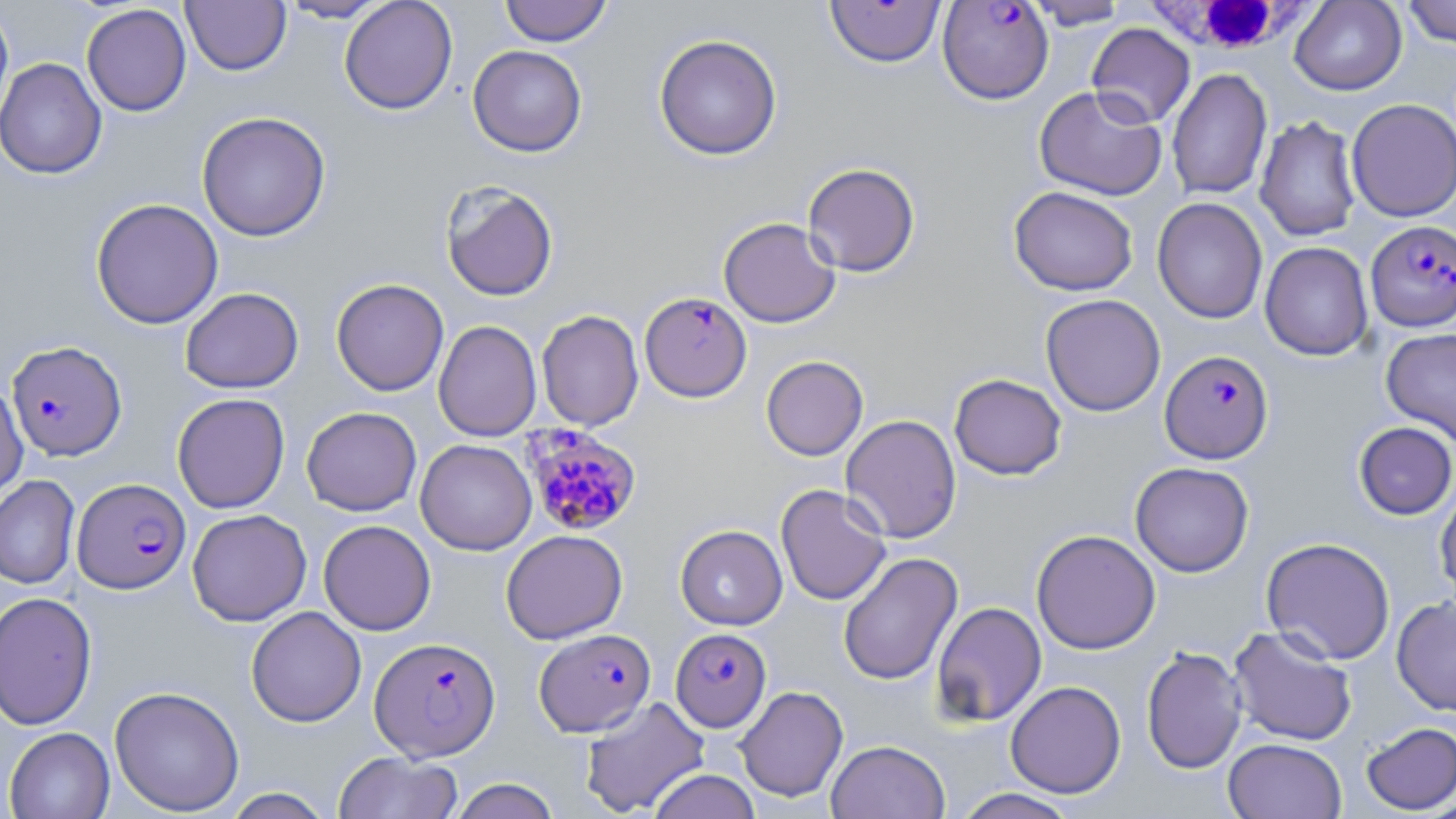

slide-level diagnosis = Plasmodium falciparum
image size = 1456×819 pixels
magnification = 1000x
field of view = one of a larger specimen
white blood cell locations = approximate bounding boxes as (x1,y1)-(x2,y2) corner pairs in pixels: (1136,0)-(1317,59)
Plasmodium falciparum-infected red blood cell locations = approximate bounding boxes as (x1,y1)-(x2,y2) corner pairs in pixels: (824,0)-(945,68), (937,1)-(1053,104), (1364,216)-(1455,327), (640,292)-(751,401), (7,340)-(126,461), (1159,350)-(1273,463), (521,423)-(642,535), (72,477)-(191,594), (671,627)-(771,732), (534,628)-(656,737), (370,636)-(500,761)
preparation = thin blood film
uninfected red blood cell locations = approximate bounding boxes as (x1,y1)-(x2,y2) corner pairs in pixels: (278,0)-(391,23), (339,0)-(457,114), (500,0)-(613,46), (1023,0)-(1130,29), (1290,0)-(1407,95), (1402,0)-(1456,47), (180,1)-(291,75), (0,3)-(14,129), (81,3)-(192,116), (1087,23)-(1195,128), (654,34)-(782,160), (468,45)-(587,157), (0,58)-(107,179), (1167,67)-(1272,200), (1034,85)-(1167,200), (1346,98)-(1456,222), (196,111)-(331,241), (1255,115)-(1361,242), (802,162)-(921,277), (439,181)-(559,302), (1009,186)-(1138,296), (1152,197)-(1268,324), (90,198)-(223,329), (718,217)-(840,328), (1259,242)-(1373,360), (331,278)-(449,396), (180,287)-(304,394), (1040,294)-(1166,416), (536,310)-(643,431), (433,320)-(541,442), (1380,327)-(1456,446), (761,355)-(868,460), (949,373)-(1067,480), (0,381)-(28,501), (172,393)-(290,513), (301,406)-(421,516), (841,414)-(962,543), (1354,422)-(1456,520), (415,438)-(537,555), (1130,462)-(1254,577), (0,475)-(80,590), (1435,482)-(1456,604), (776,484)-(891,606), (187,509)-(312,626), (318,520)-(436,635), (675,525)-(787,630), (501,529)-(628,644), (1031,529)-(1160,654), (1260,536)-(1396,663), (838,552)-(963,685), (0,591)-(97,730), (1391,595)-(1456,716), (932,601)-(1047,727), (246,606)-(366,727), (1228,625)-(1358,747), (1141,646)-(1248,774), (1005,681)-(1126,798), (735,685)-(849,803), (109,686)-(245,816), (580,696)-(710,817), (1360,721)-(1456,815), (4,727)-(115,819), (1223,738)-(1346,819), (826,740)-(950,818), (333,751)-(463,819), (647,769)-(762,819), (449,777)-(561,819), (220,788)-(334,818), (953,788)-(1081,819)
stain = May-Grünwald-Giemsa
modality = light microscopy